Locate every Plasmodium parasite.
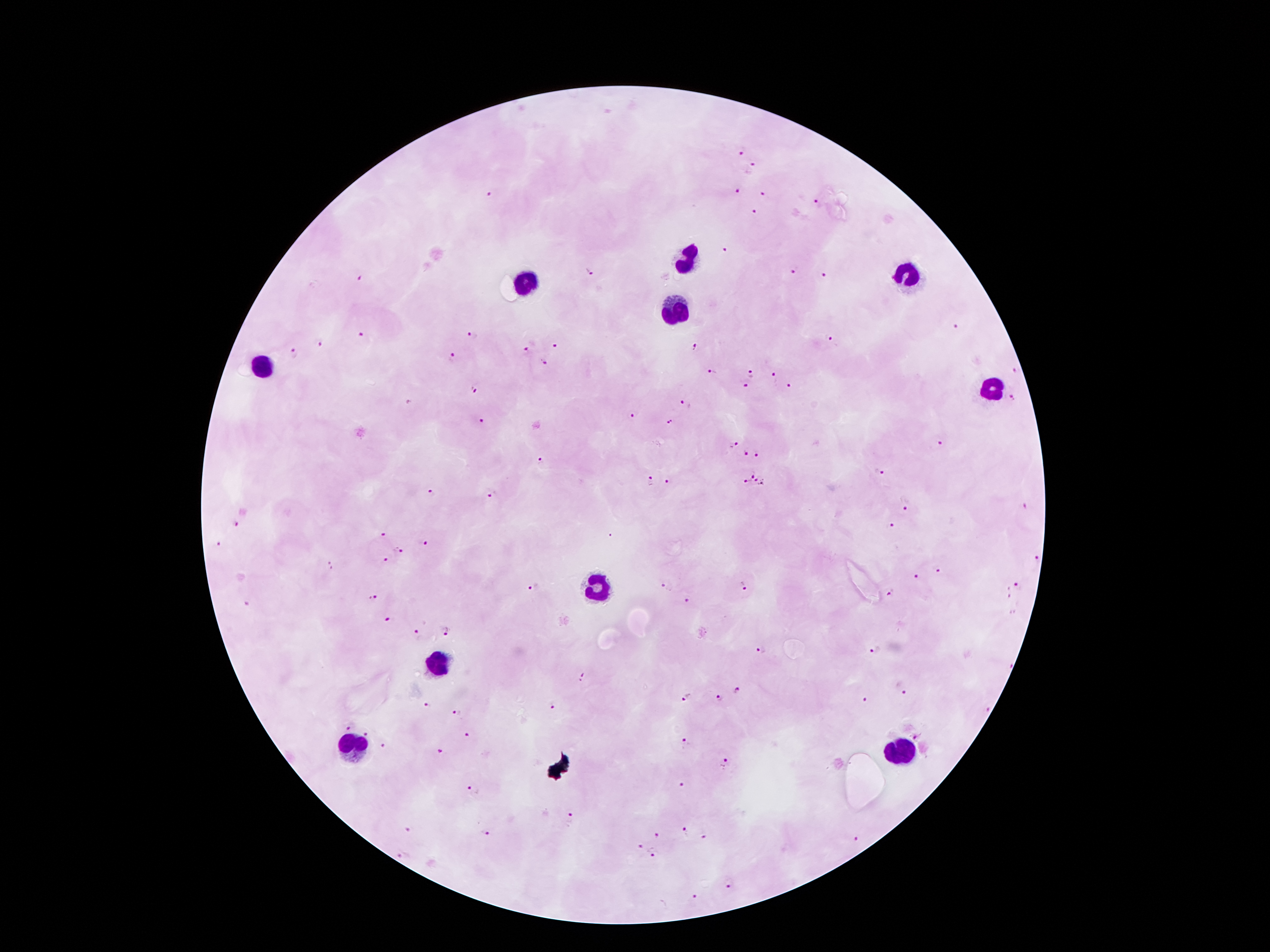

Approximate centers as (x, y) in pixels.
Plasmodium parasites: (741, 148), (753, 167), (738, 191), (763, 193), (491, 195), (819, 204), (752, 214), (724, 247), (794, 269), (588, 271), (826, 275), (363, 281), (956, 327), (472, 335), (360, 336), (831, 339), (320, 344), (554, 347), (694, 347), (526, 351), (294, 352), (451, 358), (546, 363), (1015, 371), (713, 372), (751, 374), (773, 377), (745, 386), (787, 387), (475, 388), (1013, 397), (686, 404), (634, 416), (479, 420), (669, 424), (941, 443), (734, 445), (744, 453), (757, 454), (541, 462), (751, 471), (880, 472), (651, 480), (669, 481), (745, 481), (754, 481), (762, 484), (432, 490), (492, 492), (906, 507), (1025, 507), (233, 525), (891, 525), (383, 533), (612, 535), (424, 542), (218, 543), (399, 548), (1038, 559), (387, 561), (330, 562), (938, 570), (916, 575), (1016, 584), (534, 585), (665, 585), (743, 589), (892, 593), (373, 599), (688, 599), (387, 622), (445, 630), (417, 636), (876, 648), (761, 650), (1009, 665), (584, 676), (737, 690), (900, 690), (685, 697), (719, 700), (867, 700), (553, 702), (427, 705), (986, 709), (456, 713), (349, 727), (366, 734), (914, 734), (467, 735), (685, 742), (383, 745), (441, 750), (725, 764), (683, 785), (473, 790), (570, 819), (408, 828), (487, 832), (685, 832), (658, 835), (705, 835), (856, 841), (641, 845), (653, 854), (403, 856), (729, 884), (697, 898).

Summary:
  - Leukocyte locations: (688, 260), (909, 274), (530, 282), (676, 312), (262, 367), (989, 392), (600, 586), (438, 666), (352, 747), (897, 751)
  - Field of view: single
  - Stain: Giemsa
  - Capture: smartphone through the microscope eyepiece
  - Image size: 1270×952 pixels
  - Patient malaria status: infected with Plasmodium falciparum
  - Magnification: 100x
  - Preparation: thick blood film